Outline each Plasmodium falciparum parasite and classify it by life-cycle stage.
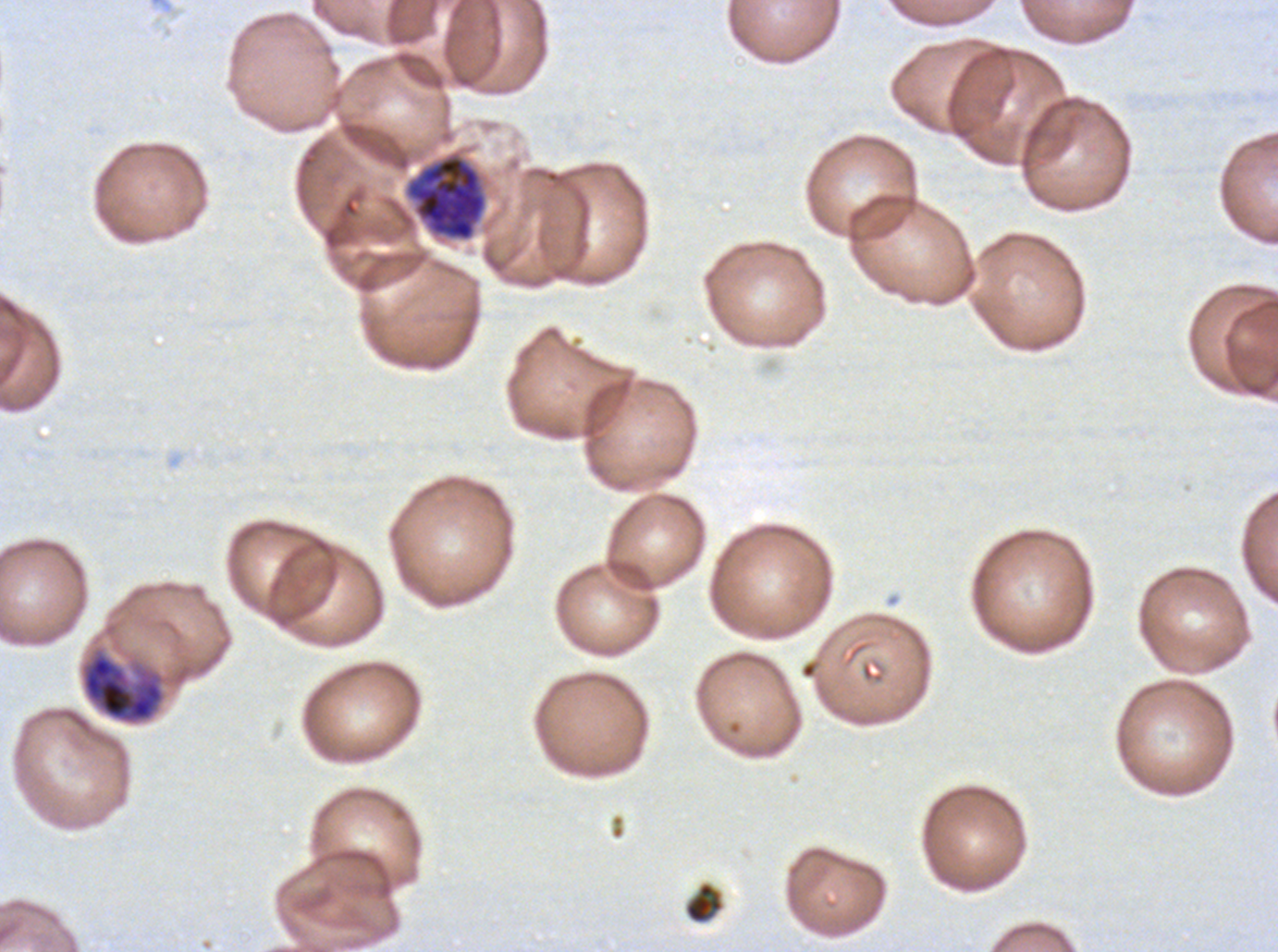

Approximate bounding rectangles given as corner coordinates in pixels from the top-left.
Late trophozoites: (x1=80, y1=647, x2=166, y2=726).
Late schizonts: (x1=404, y1=152, x2=487, y2=242).
No rings, late-ring/early-trophozoite forms, mid trophozoites, early schizonts, segmenters, or gametocytes observed.

Summary:
  - Debris locations: (x1=683, y1=881, x2=724, y2=924)
  - Specimen: Plasmodium falciparum from a patient in The Gambia, cultured ex vivo for 24 to 48 hours
  - Stain: Giemsa
  - Image size: 1278×952 pixels
  - Preparation: thin blood smear
  - Life-cycle stages observed: late trophozoite, late schizont
  - Field of view: sub-image separated from a larger composite